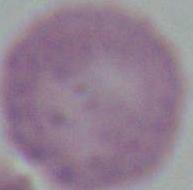
Captured at 1000x magnification. Micrograph. A red blood cell is seen.